Describe the morphology of the red blood cells.
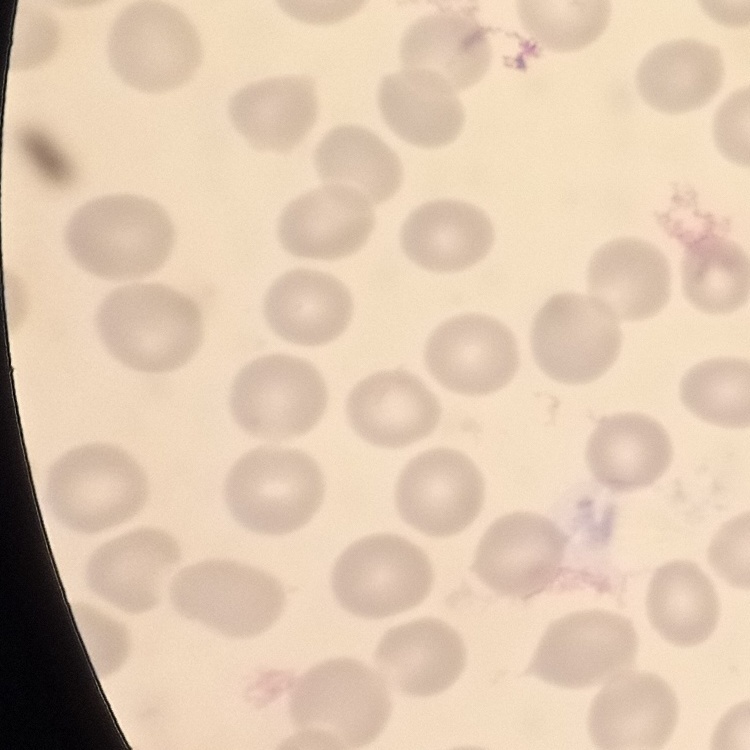

No rouleaux formation.

image_type: square crop of a larger photomicrograph
preparation: thin peripheral smear
stain: Field's or Giemsa